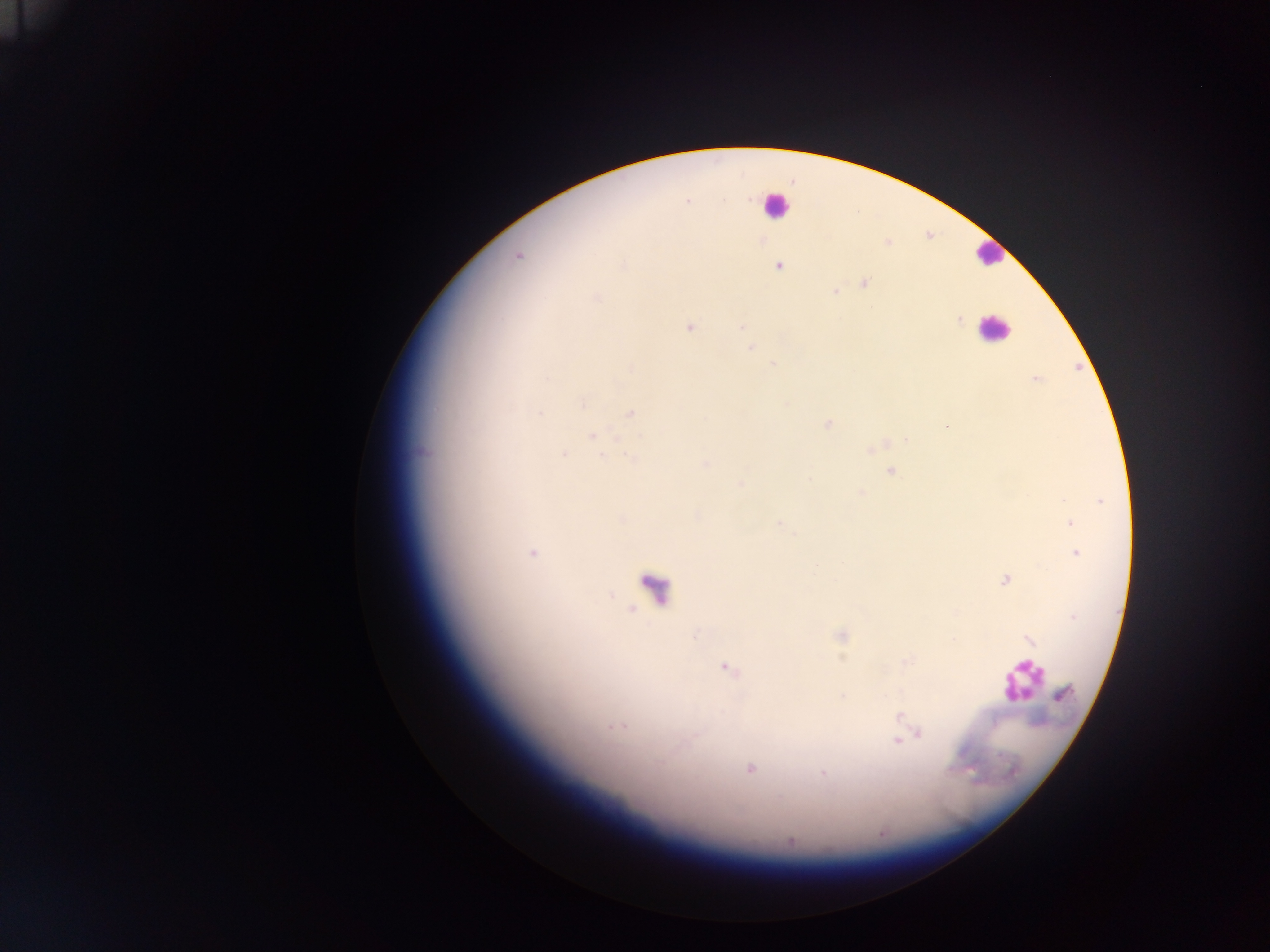
Approximate centers as [x, y] in pixels.
Summary:
  - Malaria parasite locations: [687, 202], [518, 256], [622, 266], [779, 266], [863, 282], [835, 292], [597, 299], [959, 319], [741, 326], [690, 327], [750, 348], [774, 364], [631, 368], [1035, 379], [582, 403], [540, 413], [631, 413], [828, 423], [946, 427], [592, 436], [906, 439], [422, 452], [564, 453], [602, 455], [632, 458], [705, 464], [891, 471], [809, 479], [741, 484], [860, 493], [1063, 500], [1100, 501], [1070, 523], [780, 524], [1076, 552], [532, 553], [835, 579], [1004, 580], [842, 636], [1029, 639], [727, 669], [1062, 694], [842, 696], [900, 715], [611, 727], [620, 727], [918, 734], [897, 741], [660, 762], [750, 769], [823, 772], [790, 841]
  - Leukocyte locations: [776, 206], [988, 253], [993, 329], [657, 590], [1021, 680]
  - Image size: 1270×952 pixels
  - Field of view: single
  - Capture: mobile-phone photograph through a microscope
  - Preparation: thick blood smear
  - Country: Ghana